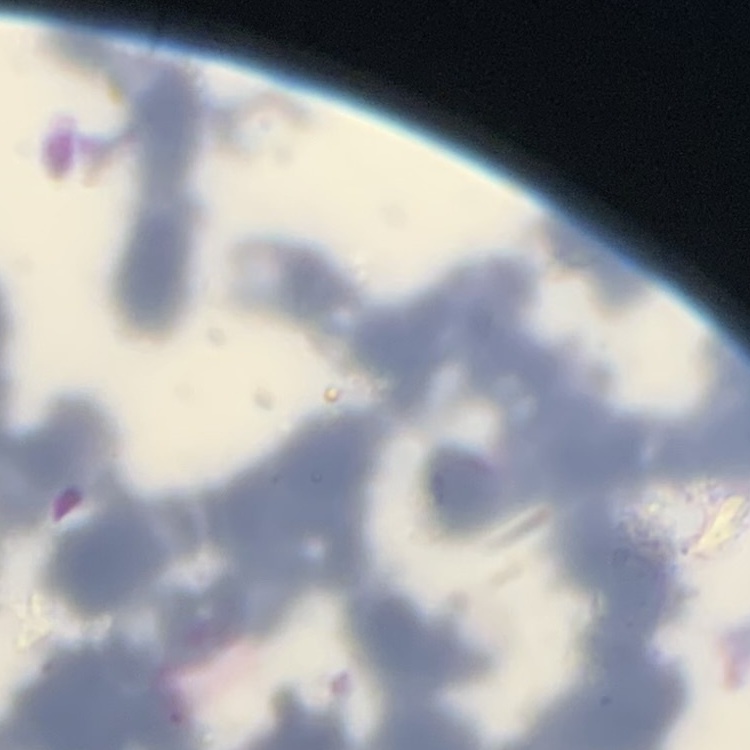

Summary:
  - Red blood cell morphology: rouleaux formation
  - Stain: Field's or Giemsa
  - Image type: one tile cut from a larger photomicrograph
  - Preparation: thin blood film